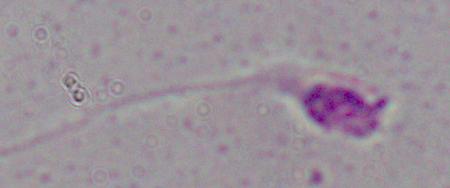
identification = Leishmania
modality = photomicrograph
magnification = 1000x